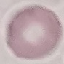
{
  "malaria_status": "uninfected",
  "preparation": "thin blood film",
  "image_type": "cell patch, automatically extracted from a larger field of view and resized to 64 × 64 pixels",
  "capture": "smartphone camera at the microscope eyepiece",
  "stain": "Giemsa"
}